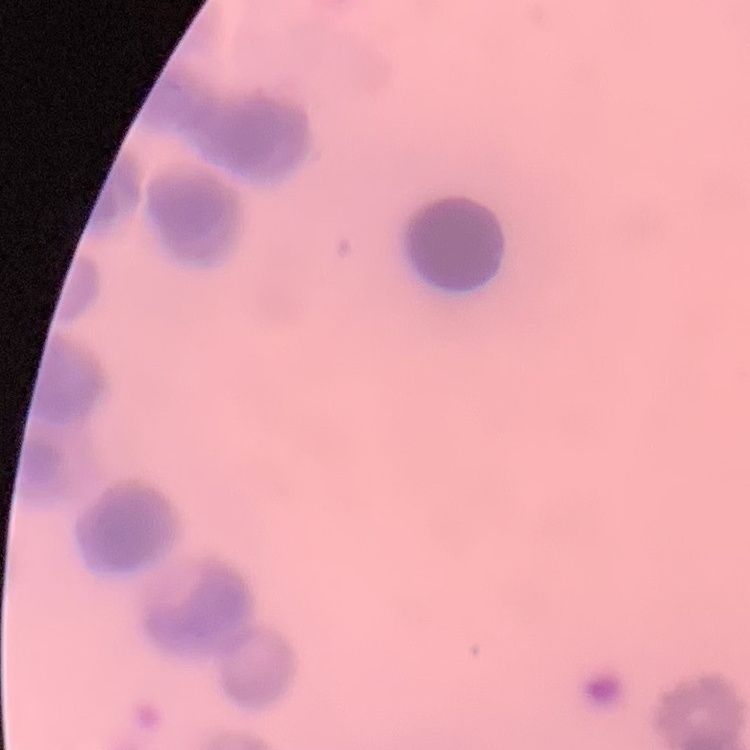
The red blood cells exhibit rouleaux formation. Square crop of a larger photomicrograph. Thin peripheral smear. Field's or Giemsa stain.